Assess this cell for malaria.
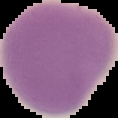

It is uninfected.

image type = cell region segmented out of the field of view; surrounding area masked to black
preparation = thin blood film
image size = 118×118 pixels